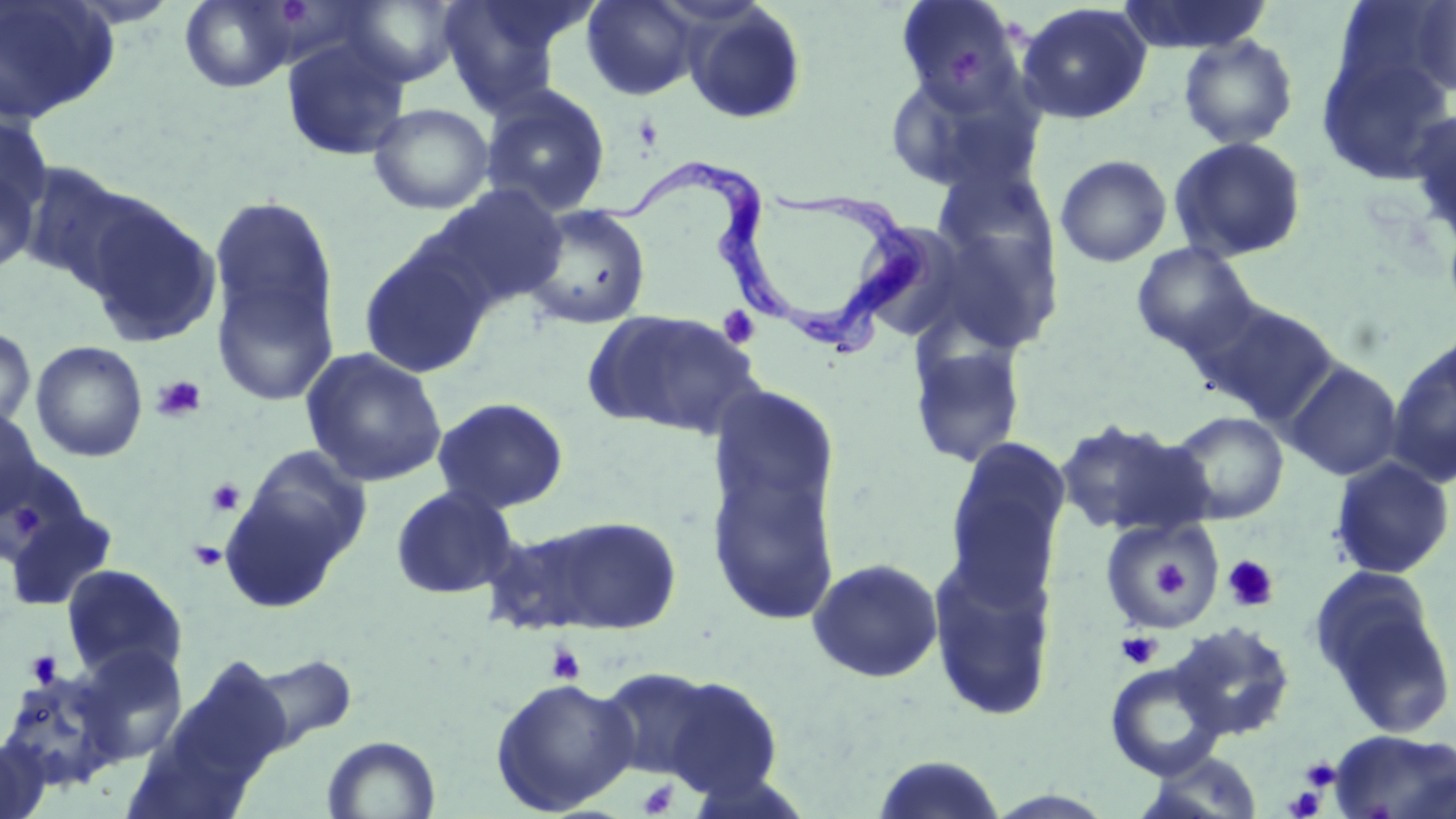
Trypanosoma brucei locations = approximate bounding boxes as [x1, y1, x2, y2] in pixels: [584, 157, 798, 319], [778, 182, 928, 355]
slide-level diagnosis = Trypanosoma brucei
image size = 1456×819 pixels
platelet locations = approximate bounding boxes as [x1, y1, x2, y2] in pixels: [633, 113, 664, 151], [718, 305, 761, 350], [151, 375, 208, 423], [205, 478, 245, 517], [13, 508, 43, 534], [187, 540, 228, 572], [1145, 554, 1190, 601], [1222, 555, 1279, 612], [1117, 632, 1161, 669], [546, 644, 586, 684], [25, 650, 63, 688], [1301, 757, 1340, 790], [637, 779, 678, 817], [1284, 787, 1326, 818]
magnification = 1000x
stain = May-Grünwald-Giemsa
preparation = thin blood smear
uninfected red blood cell locations = approximate bounding boxes as [x1, y1, x2, y2] in pixels: [0, 0, 120, 124], [178, 0, 303, 93], [341, 0, 463, 87], [438, 0, 578, 112], [581, 0, 702, 100], [895, 0, 1027, 112], [1117, 0, 1272, 54], [1409, 1, 1456, 97], [1016, 2, 1153, 125], [683, 3, 808, 126], [1178, 34, 1299, 150], [280, 36, 411, 162], [1315, 42, 1456, 185], [881, 68, 1037, 193], [480, 84, 612, 217], [367, 103, 495, 215], [1407, 107, 1456, 248], [0, 109, 54, 236], [1168, 136, 1308, 263], [1054, 154, 1172, 268], [0, 161, 42, 276], [15, 161, 151, 292], [424, 184, 569, 314], [209, 195, 339, 345], [82, 197, 222, 348], [520, 204, 653, 330], [918, 220, 1064, 357], [853, 221, 976, 342], [358, 242, 493, 379], [1130, 242, 1260, 359], [210, 263, 341, 408], [1194, 299, 1341, 429], [583, 309, 762, 440], [0, 325, 36, 431], [908, 339, 1027, 468], [30, 340, 148, 462], [1385, 344, 1456, 486], [301, 348, 448, 488], [1283, 361, 1404, 482], [703, 389, 842, 632], [431, 397, 569, 514], [0, 409, 47, 518], [1168, 411, 1289, 524], [1055, 418, 1210, 538], [943, 436, 1072, 602], [220, 446, 372, 610], [0, 457, 86, 565], [1328, 457, 1454, 580], [390, 485, 519, 599], [3, 501, 119, 613], [530, 515, 684, 635], [1100, 518, 1227, 634], [478, 521, 627, 636], [927, 554, 1058, 725], [806, 557, 944, 684], [60, 564, 188, 682], [1311, 574, 1455, 738], [1170, 621, 1295, 742], [73, 644, 189, 764], [241, 651, 358, 751], [173, 657, 293, 782], [1105, 663, 1225, 780], [594, 666, 729, 785], [0, 670, 120, 791], [649, 673, 784, 799], [489, 675, 639, 816], [1329, 730, 1456, 819], [322, 735, 441, 818], [0, 736, 50, 819], [1134, 751, 1266, 819], [871, 755, 1007, 819]
modality = optical microscopy
field of view = single